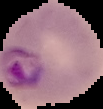

From a thin blood smear. Image is 103×109 pixels. The area outside the segmented cell region is set to black. Malaria status: parasitized.